State which parasite is depicted.
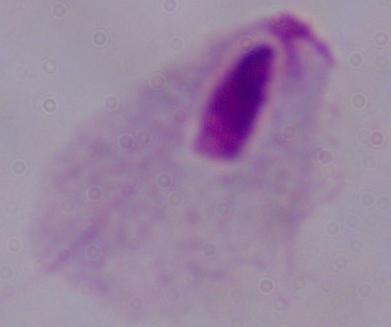

A trichomonad.

Photomicrograph. Captured at 1000x magnification.